Name the cell type shown.
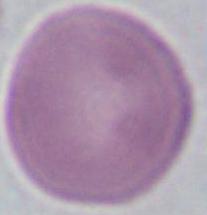

This is an erythrocyte.

{
  "magnification": "1000x",
  "modality": "micrograph"
}